Assess the morphology of the erythrocytes.
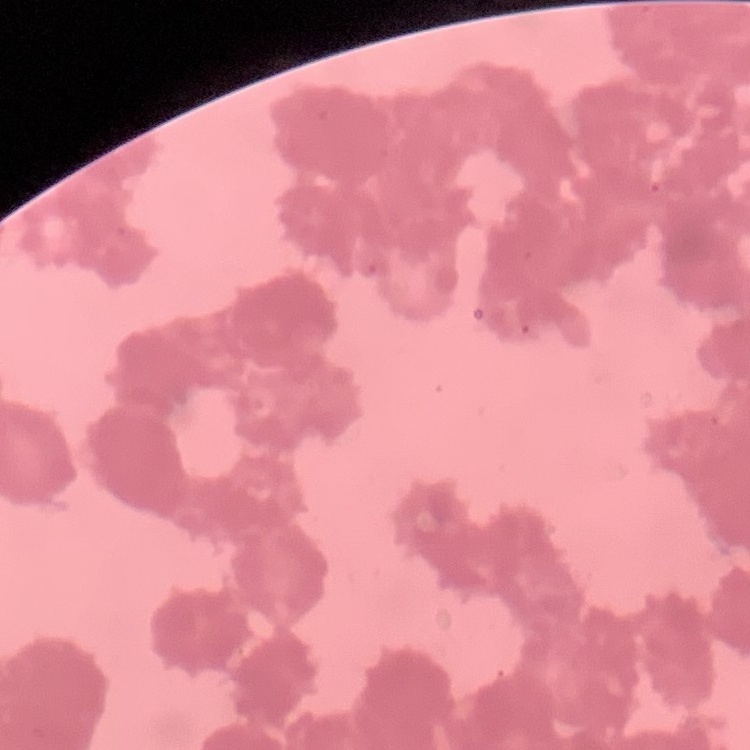
They show rouleaux formation.

Summary:
  - Preparation: thin blood smear
  - Stain: Field's or Giemsa
  - Image type: square crop of a larger photomicrograph